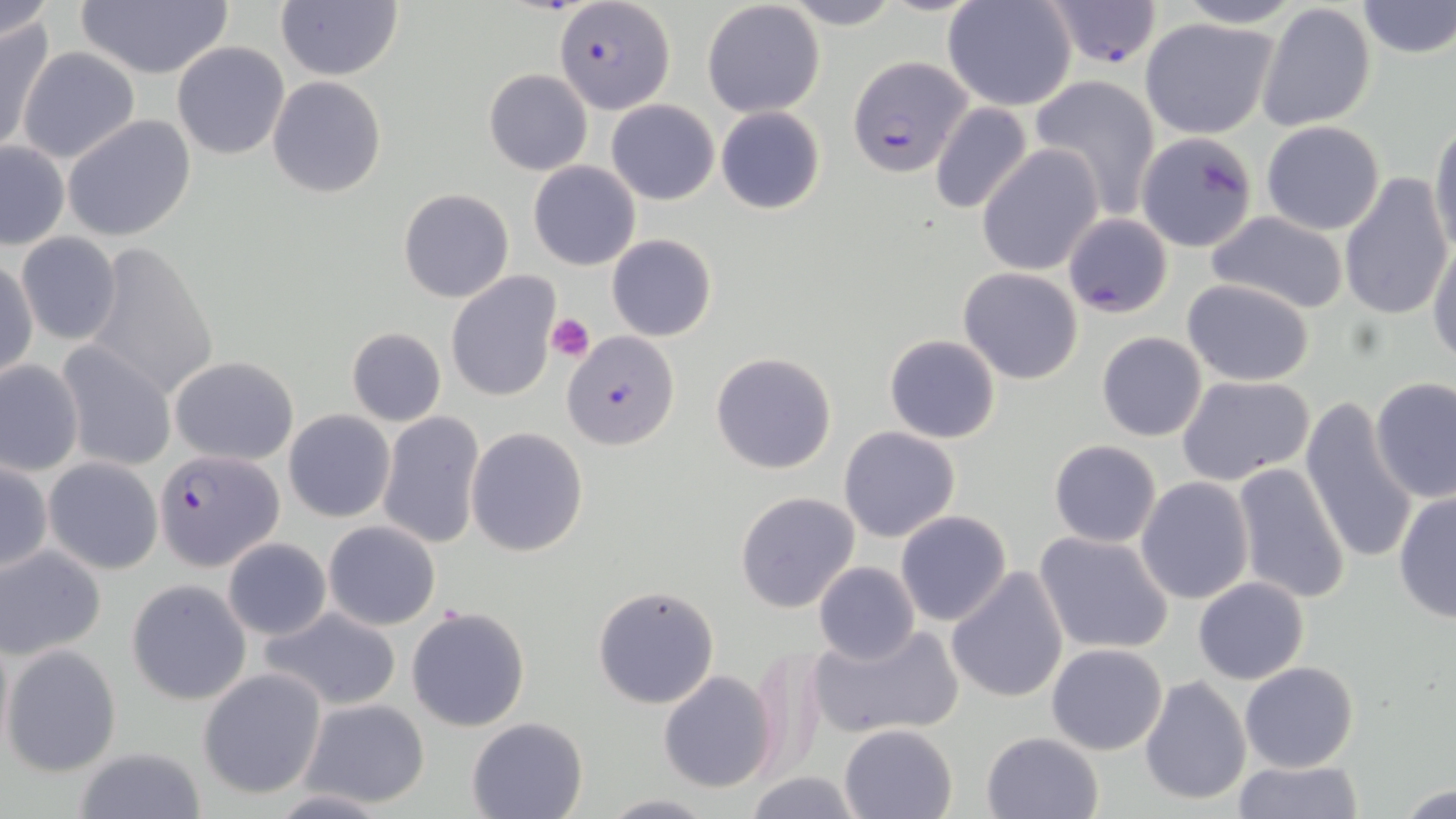
Summary:
  - Coordinate format: approximate bounding boxes as (x1, y1, x2, y2) in pixels
  - Platelet locations: (546, 312, 594, 360)
  - Plasmodium falciparum-infected red blood cell locations: (554, 2, 676, 114), (1044, 2, 1163, 68), (849, 54, 975, 177), (154, 448, 284, 574)
  - Uninfected red blood cell locations: (0, 0, 54, 44), (779, 0, 903, 30), (942, 0, 1078, 112), (1169, 0, 1304, 28), (74, 1, 233, 79), (275, 1, 403, 81), (701, 1, 826, 117), (1355, 1, 1456, 59), (1257, 2, 1377, 132), (0, 17, 52, 155), (1140, 17, 1278, 139), (172, 41, 290, 159), (17, 47, 140, 164), (35, 51, 166, 239), (483, 68, 594, 175), (1031, 74, 1161, 217), (267, 76, 387, 199), (606, 100, 720, 205), (929, 102, 1034, 216), (715, 106, 826, 215), (63, 115, 197, 242), (1430, 119, 1456, 259), (1259, 120, 1385, 234), (1135, 132, 1257, 252), (1291, 142, 1435, 288), (0, 143, 70, 250), (977, 146, 1103, 275), (528, 160, 641, 271), (1338, 172, 1451, 322), (399, 188, 514, 304), (1203, 210, 1353, 315), (1063, 213, 1175, 320), (15, 233, 122, 345), (607, 234, 717, 341), (1428, 234, 1456, 367), (81, 239, 222, 403), (1, 256, 38, 382), (958, 267, 1084, 385), (446, 271, 561, 403), (1180, 279, 1316, 385), (346, 327, 447, 427), (562, 331, 680, 449), (1096, 331, 1207, 442), (884, 334, 1001, 443), (57, 342, 175, 472), (710, 351, 838, 475), (170, 356, 298, 463), (0, 359, 85, 477), (1176, 374, 1317, 488), (1371, 377, 1456, 503), (1300, 398, 1418, 565), (284, 410, 395, 523), (378, 411, 484, 549), (839, 426, 962, 543), (466, 427, 589, 557), (1049, 440, 1161, 547), (44, 456, 162, 575), (0, 460, 50, 577), (1231, 461, 1352, 605), (1136, 477, 1254, 605), (1392, 489, 1456, 624), (733, 490, 860, 614), (896, 510, 1012, 627), (324, 521, 440, 631), (1031, 529, 1177, 657), (224, 538, 331, 640), (0, 545, 106, 659), (814, 562, 920, 664), (945, 566, 1071, 705), (1193, 576, 1310, 684), (126, 579, 251, 705), (593, 585, 720, 709), (406, 604, 532, 733), (261, 606, 403, 711), (806, 623, 963, 742), (747, 642, 829, 780), (2, 643, 122, 777), (1046, 643, 1168, 755), (1239, 661, 1360, 772), (198, 668, 326, 798), (657, 671, 777, 793), (1138, 675, 1251, 808), (298, 697, 432, 808), (466, 717, 589, 819), (839, 723, 957, 818), (980, 730, 1103, 818), (68, 746, 205, 819), (1232, 759, 1363, 817), (745, 771, 864, 819), (1394, 782, 1456, 818), (600, 794, 715, 819)
  - Slide-level diagnosis: Plasmodium falciparum
  - Image size: 1456×819 pixels
  - Stain: May-Grünwald-Giemsa
  - Modality: optical microscopy
  - Field of view: one of a larger specimen
  - Magnification: 1000x
  - Preparation: thin blood film